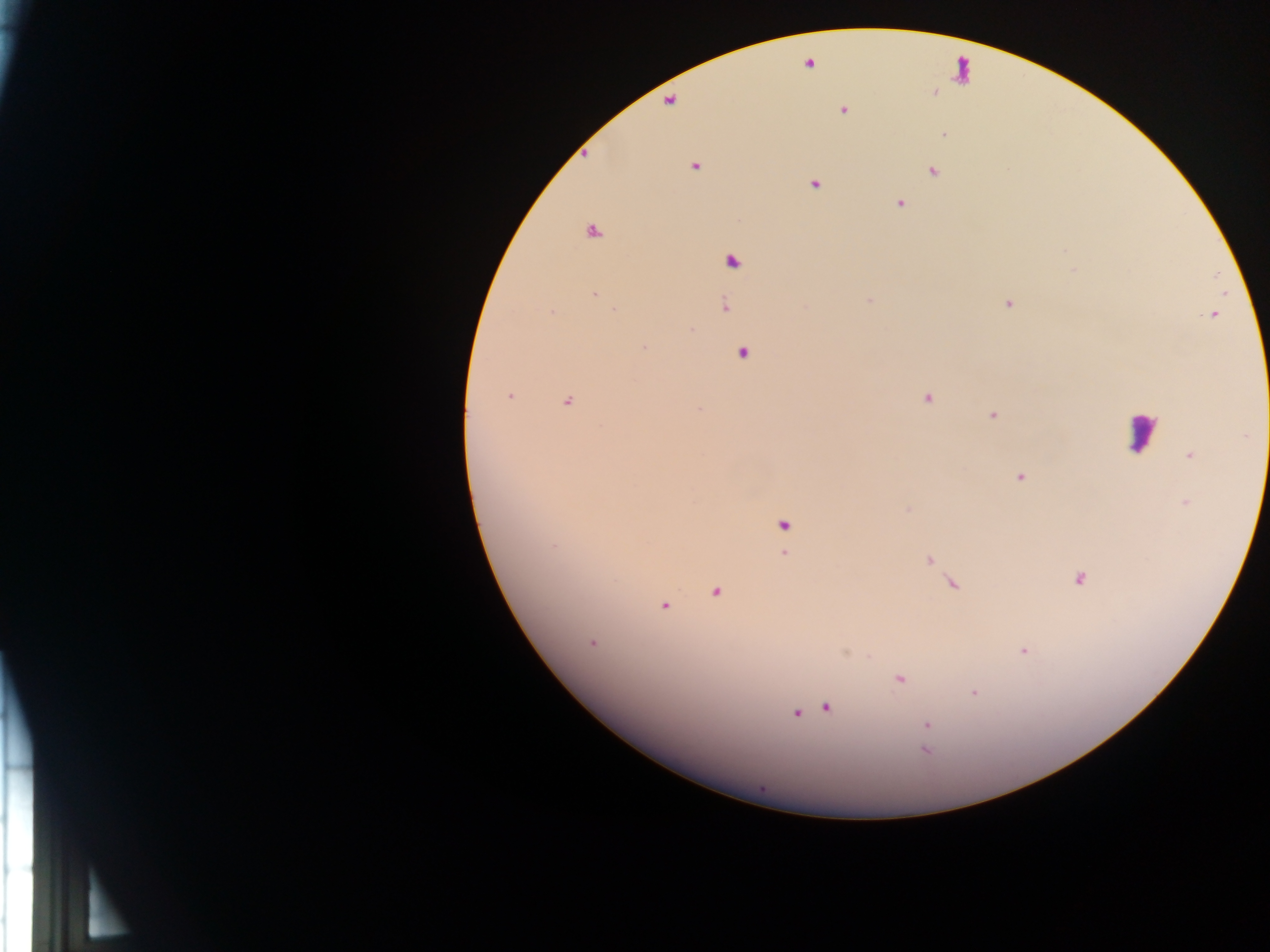 Approximate centers as {x, y} in pixels. Malaria parasite locations: {809, 63}, {843, 110}, {944, 134}, {695, 167}, {933, 170}, {814, 184}, {899, 203}, {592, 232}, {732, 261}, {594, 294}, {869, 300}, {1008, 303}, {724, 307}, {615, 310}, {552, 311}, {644, 348}, {742, 352}, {509, 396}, {927, 398}, {568, 401}, {993, 415}, {1190, 456}, {1020, 477}, {1185, 502}, {908, 508}, {783, 526}, {554, 546}, {784, 554}, {929, 560}, {1078, 579}, {954, 585}, {716, 592}, {664, 605}, {592, 642}, {1024, 651}, {900, 679}, {974, 693}, {826, 708}, {796, 713}, {927, 725}, {927, 736}, {925, 751}. Leukocyte locations (subset; some below the resolvable size): {1141, 432}. Thick blood film. Image is 1270×952 pixels. One field of view. Sample from Ghana. Mobile-phone photograph taken through the microscope.